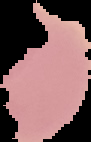
preparation = thin blood smear
image type = segmented cell region on a black background
malaria status = uninfected
image size = 91×142 pixels